Assess this cell for malaria.
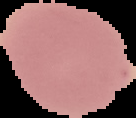

It is uninfected.

Summary:
  - Image size: 136×118 pixels
  - Image type: cell region segmented out of the field of view; surrounding area masked to black
  - Preparation: thin blood film